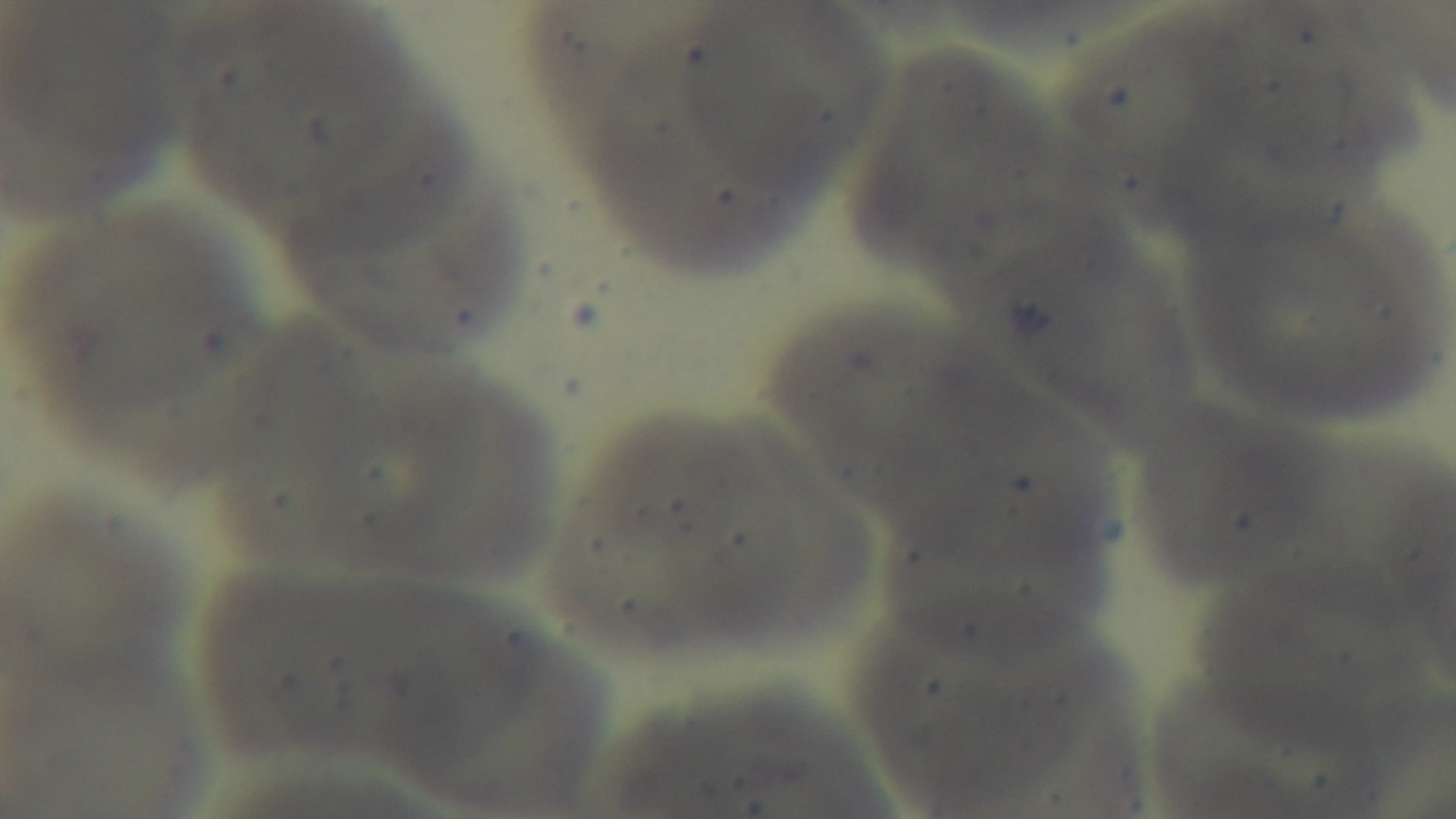
Summary:
  - Stain: Giemsa
  - Modality: light microscopy
  - Malaria status: uninfected
  - Preparation: thin blood film
  - Capture: mounted 4K digital camera
  - Objective: 100x oil immersion
  - Field of view: one from the slide